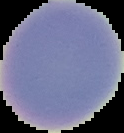
Summary:
  - Preparation: thin blood smear
  - Image size: 124×133 pixels
  - Result: negative for Plasmodium parasites
  - Image type: cell region segmented out of the field of view; surrounding area masked to black